Locate every Plasmodium parasite.
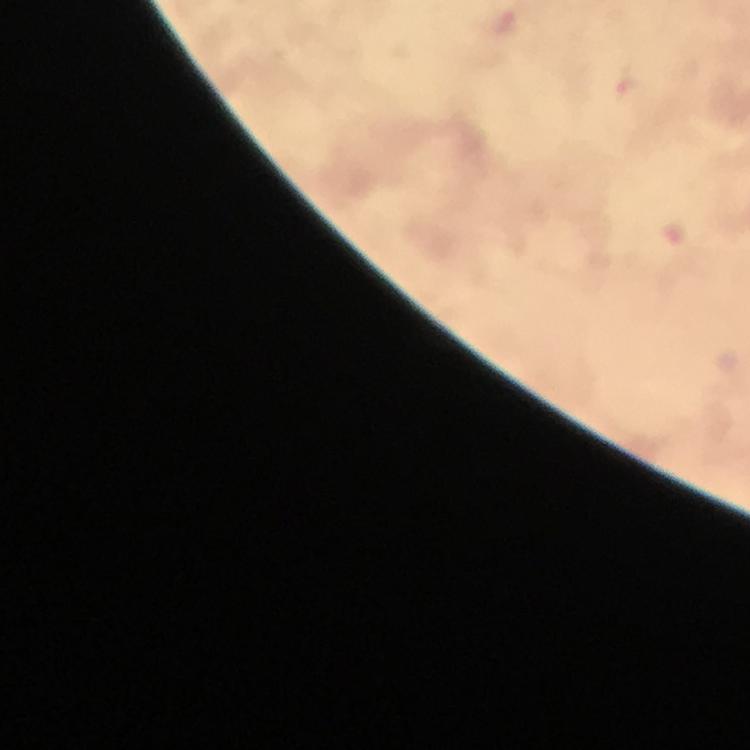

Approximate object centers, in pixels from the top-left corner.
Plasmodium parasites: (x=504, y=23), (x=629, y=88).

Thick blood smear. From a malaria diagnostic workup. Giemsa stain. 100x magnification. Image is 750×750 pixels. A crop from one field of view. Immersion oil was used. Smartphone photograph taken through a microscope.